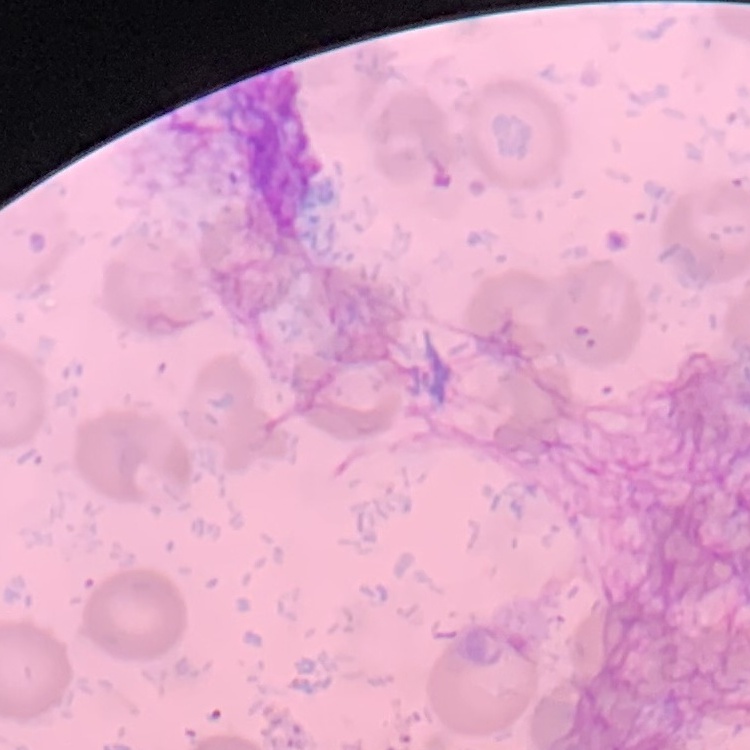
The red blood cells show no rouleaux formation. Thin blood film. Stained with either Field's or Giemsa. Square crop of a larger photomicrograph.